Point out every Plasmodium parasite.
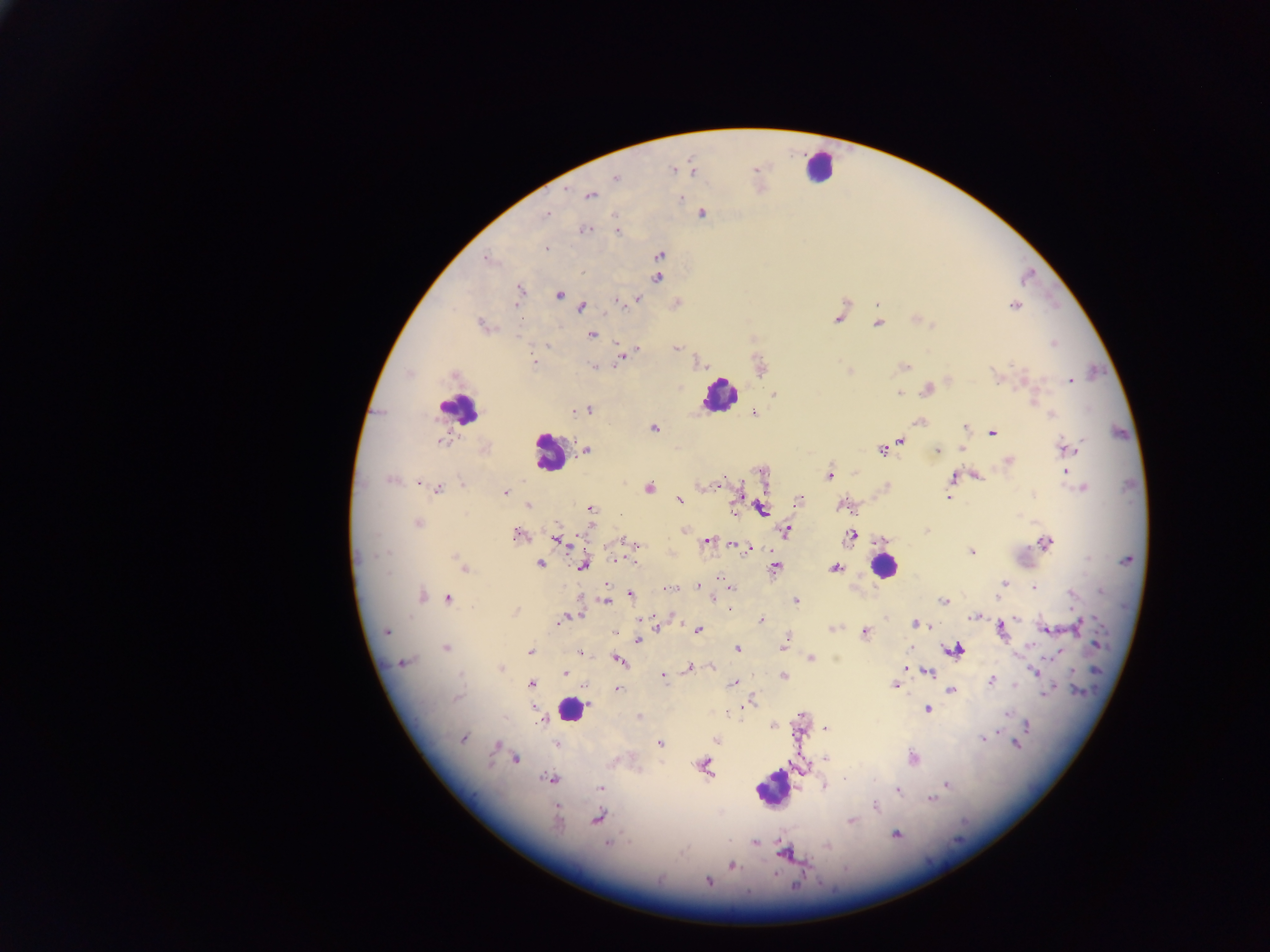

Approximate centers as [x, y] in pixels.
Plasmodium parasites: [756, 169], [673, 170], [694, 172], [614, 178], [566, 191], [592, 196], [681, 198], [547, 213], [703, 214], [585, 230], [616, 231], [545, 249], [660, 254], [490, 259], [582, 273], [658, 278], [519, 290], [561, 296], [638, 298], [615, 302], [877, 305], [1015, 306], [582, 307], [836, 320], [914, 320], [878, 324], [934, 324], [480, 326], [592, 335], [1052, 344], [545, 345], [638, 347], [676, 348], [621, 357], [535, 361], [696, 363], [1012, 364], [905, 367], [593, 368], [845, 368], [849, 370], [409, 374], [995, 376], [1025, 376], [1070, 380], [927, 389], [898, 393], [774, 394], [1037, 398], [1034, 402], [590, 408], [754, 414], [1051, 414], [918, 422], [963, 426], [655, 429], [991, 434], [442, 440], [903, 440], [886, 449], [938, 449], [587, 450], [963, 450], [1071, 450], [881, 451], [585, 455], [1008, 461], [855, 472], [1067, 472], [976, 474], [828, 475], [952, 476], [720, 479], [388, 481], [418, 482], [698, 486], [437, 488], [649, 488], [1084, 488], [504, 492], [1033, 493], [948, 497], [678, 501], [799, 501], [736, 502], [528, 504], [734, 508], [762, 508], [591, 510], [417, 523], [684, 530], [788, 530], [518, 534], [850, 535], [623, 540], [555, 541], [707, 542], [733, 544], [1044, 544], [637, 546], [971, 550], [382, 552], [372, 556], [454, 556], [363, 558], [1087, 558], [616, 560], [540, 563], [581, 565], [775, 566], [463, 568], [835, 568], [384, 574], [720, 576], [1004, 582], [1000, 585], [605, 586], [697, 586], [1033, 588], [631, 595], [423, 596], [438, 597], [448, 597], [711, 598], [942, 599], [997, 599], [606, 600], [797, 600], [730, 608], [516, 610], [564, 617], [972, 617], [672, 618], [643, 619], [761, 620], [915, 622], [1079, 624], [832, 628], [699, 629], [1003, 629], [384, 630], [655, 630], [865, 630], [1045, 630], [616, 632], [1074, 632], [786, 637], [637, 638], [783, 645], [1096, 645], [447, 647], [737, 647], [956, 650], [531, 653], [580, 653], [1054, 655], [811, 657], [618, 660], [403, 661], [689, 667], [710, 667], [502, 670], [1034, 671], [564, 673], [929, 673], [662, 676], [783, 676], [990, 680], [531, 684], [733, 684], [894, 685], [1015, 685], [617, 688], [951, 690], [1079, 691], [1045, 693], [754, 700], [588, 703], [928, 709], [725, 713], [1008, 714], [800, 716], [1027, 723], [773, 727], [825, 727], [465, 738], [986, 738], [982, 739], [716, 740], [660, 742], [1019, 744], [495, 745], [493, 751], [515, 758], [825, 759], [707, 762], [709, 769], [846, 778], [549, 779], [947, 784], [599, 788], [898, 790], [930, 800], [877, 806], [558, 817], [598, 818], [849, 820], [896, 836], [754, 843], [607, 844], [826, 844], [784, 856], [734, 866], [773, 874], [709, 882].

Summary:
  - Leukocyte locations: [820, 165], [725, 395], [456, 412], [548, 456], [883, 563], [571, 709], [774, 792]
  - Country: Ghana
  - Preparation: thick blood film
  - Image size: 1270×952 pixels
  - Capture: mobile-phone photograph through a microscope
  - Field of view: single